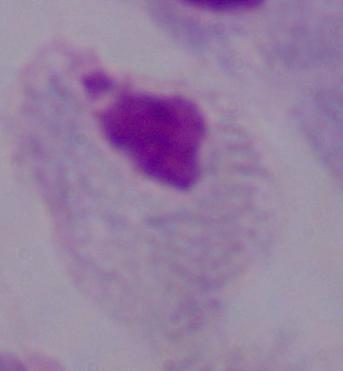 1000x magnification. Micrograph. A trichomonad is seen.